Name the blood parasite species.
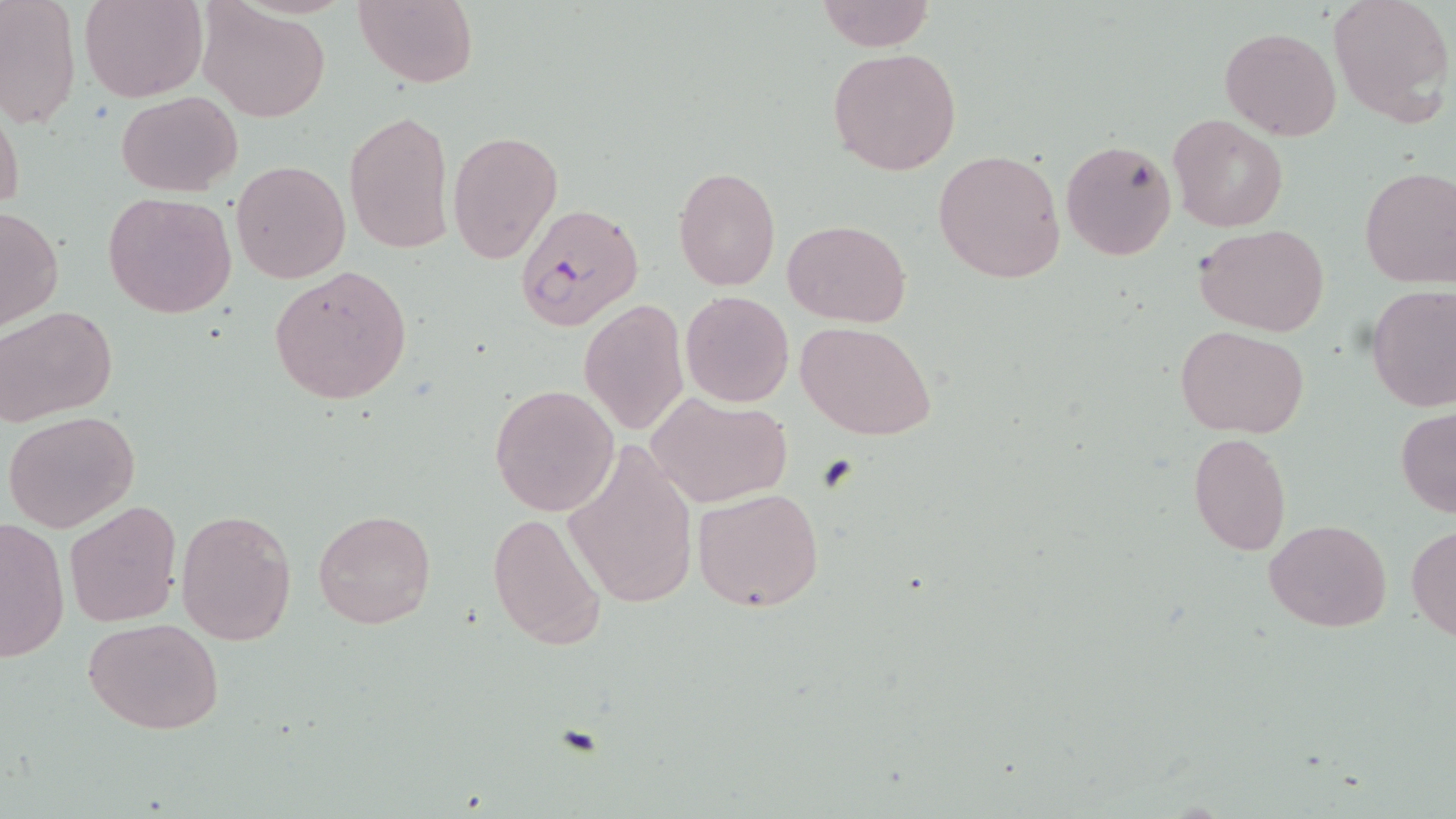

Plasmodium falciparum.

preparation: thin blood smear
plasmodium_falciparum_infected_red_blood_cell_locations: 'approximate bounding boxes as (x1, y1, x2, y2) in pixels: (513, 203, 643, 332)'
modality: light microscopy
uninfected_red_blood_cell_locations: 'approximate bounding boxes as (x1, y1, x2, y2) in pixels: (80, 0, 206, 102), (353, 0, 479, 88), (0, 1, 80, 130), (817, 1, 933, 52), (1328, 1, 1454, 125), (198, 3, 329, 121), (1219, 27, 1342, 141), (828, 47, 963, 176), (116, 91, 240, 196), (1, 102, 24, 216), (342, 108, 454, 256), (1170, 114, 1289, 232), (447, 129, 562, 266), (1061, 139, 1176, 261), (934, 148, 1065, 285), (230, 159, 351, 285), (673, 166, 780, 292), (1359, 167, 1456, 289), (103, 191, 238, 319), (0, 207, 63, 330), (782, 218, 910, 328), (1195, 224, 1330, 335), (268, 266, 413, 405), (1366, 284, 1455, 412), (680, 291, 795, 407), (577, 298, 689, 437), (1, 305, 117, 426), (796, 320, 937, 441), (1176, 326, 1311, 438), (489, 384, 619, 517), (646, 392, 792, 508), (1396, 408, 1456, 518), (4, 411, 140, 534), (1189, 431, 1292, 557), (562, 440, 699, 611), (692, 486, 824, 612), (65, 500, 181, 627), (175, 509, 297, 645), (312, 509, 435, 628), (487, 510, 609, 653), (1, 519, 70, 661), (1265, 519, 1391, 632), (1406, 526, 1456, 639), (82, 617, 225, 735)'
magnification: 1000x
image_size: 1456×819 pixels
field_of_view: single
stain: May-Grünwald-Giemsa